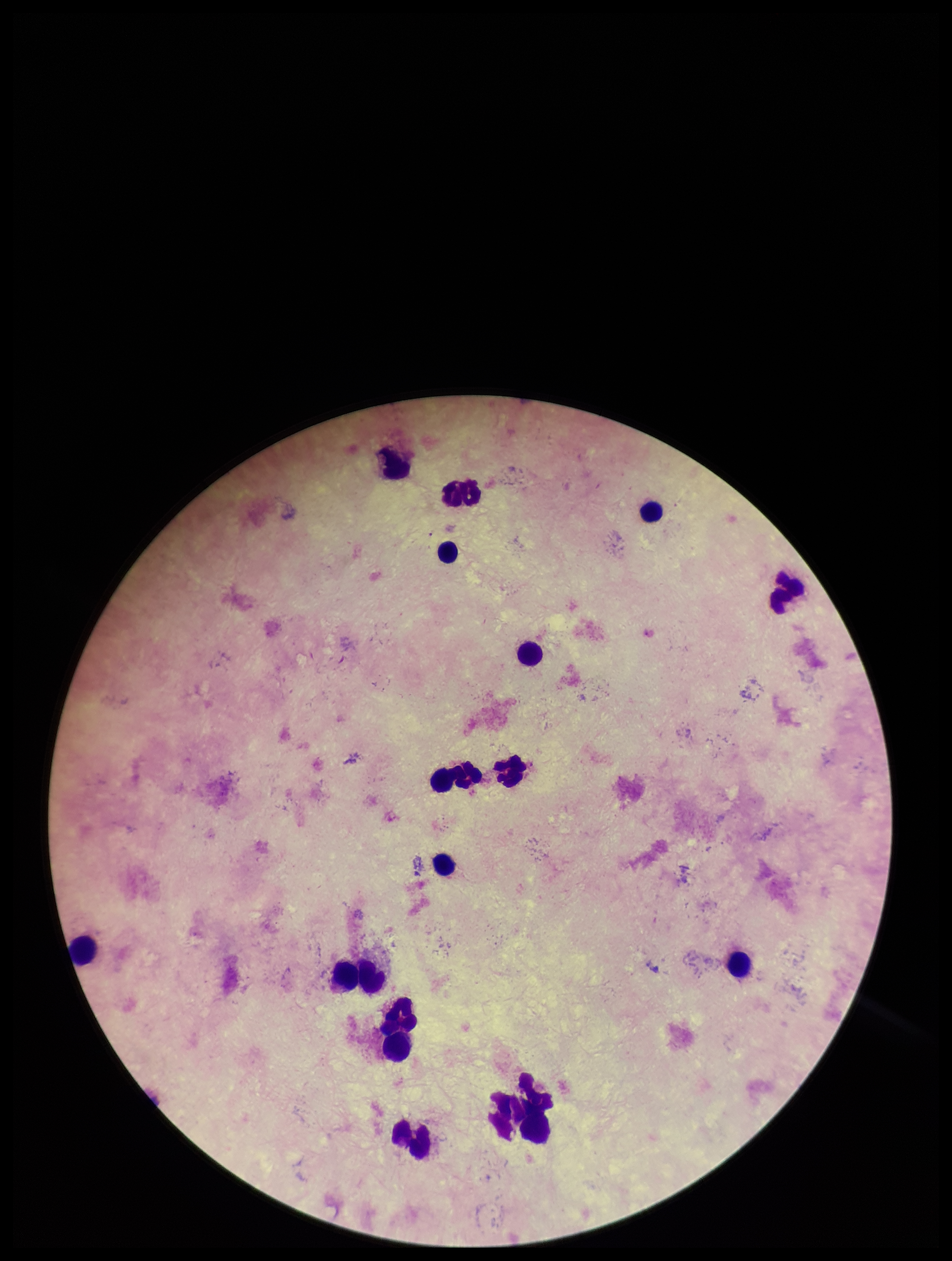
{
  "plasmodium_parasites": "none identified",
  "leukocyte_count": 15,
  "image_size": "952×1261 pixels",
  "capture": "smartphone photograph through the microscope eyepiece",
  "parasite_count": 0,
  "patient_malaria_status": "negative",
  "preparation": "thick blood smear",
  "field_of_view": "single",
  "stain": "Giemsa"
}